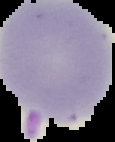 Image is 115×142 pixels. From a thin blood smear. Segmented cell region on a black background. Result: no Plasmodium parasites detected.